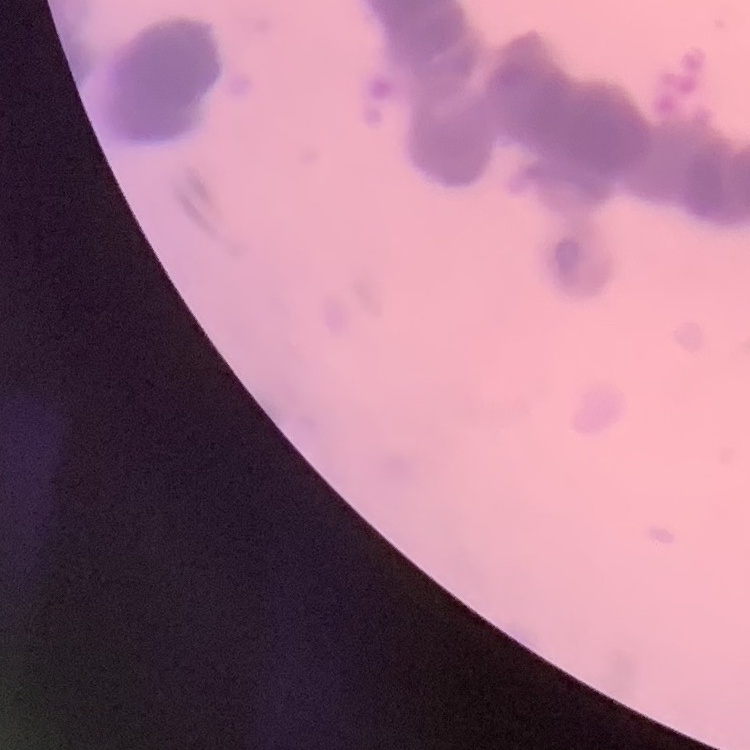

Summary:
  - Erythrocyte morphology: rouleaux formation
  - Image type: square crop of a larger photomicrograph
  - Preparation: thin blood smear
  - Stain: Field's or Giemsa